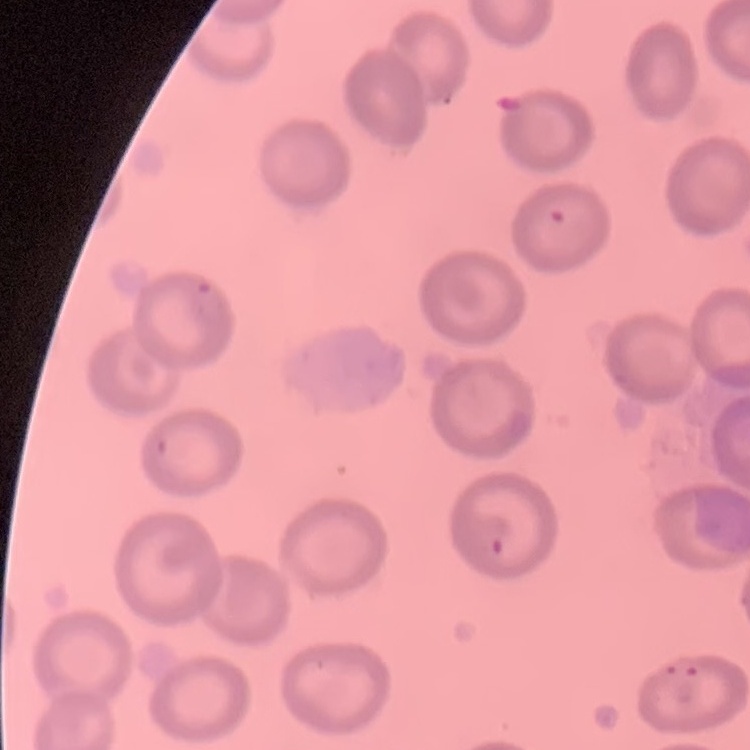

erythrocyte morphology = no rouleaux formation
preparation = thin blood smear
image type = one tile cut from a larger photomicrograph
stain = Field's or Giemsa